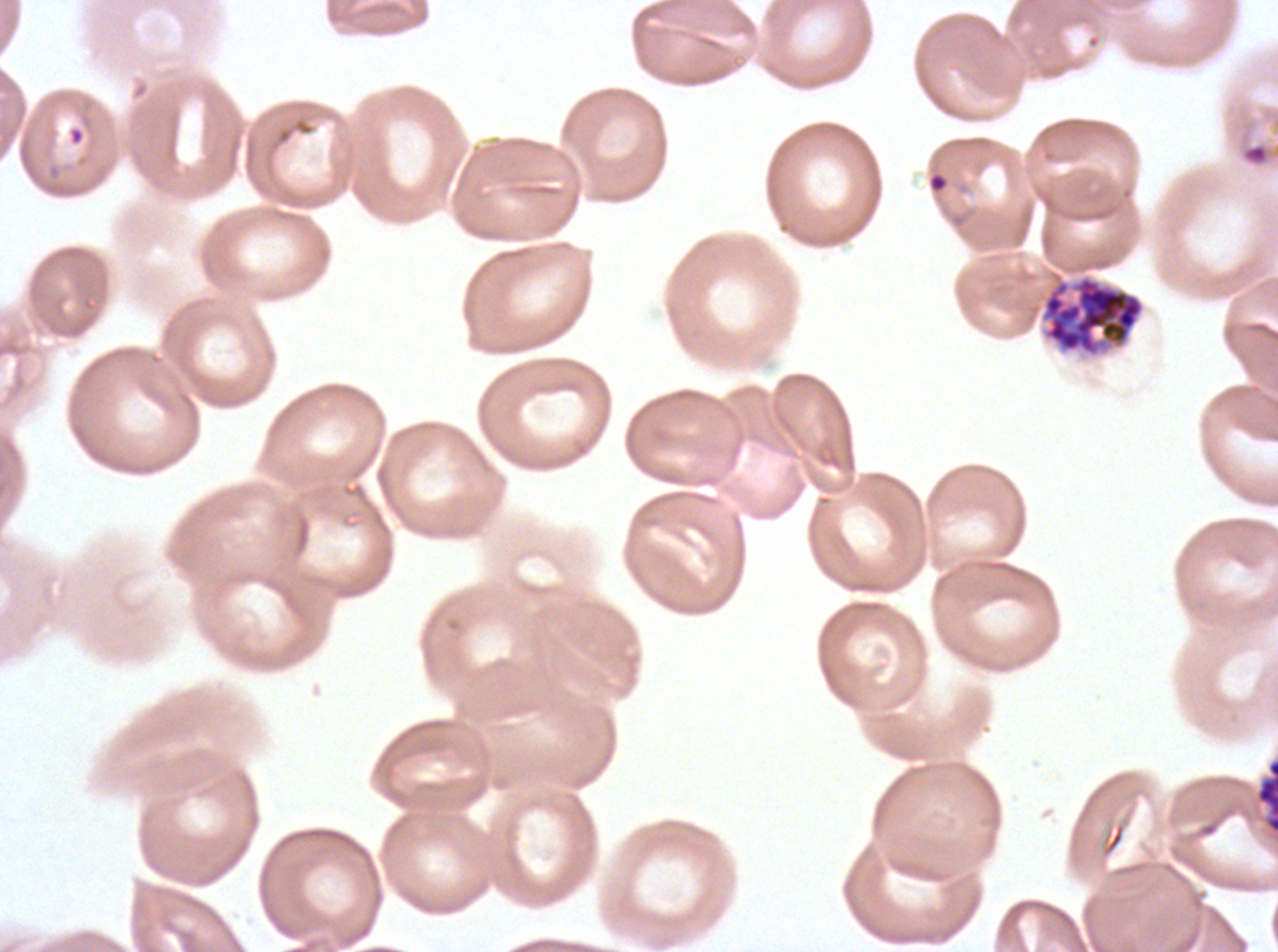

Approximate bounding boxes as {x1, y1, x2, y2} in pixels. Late schizont locations: {1255, 758, 1277, 835}. Ring locations: {927, 171, 949, 194}. Debris locations: {1238, 140, 1277, 169}. Segmenter locations: {1039, 271, 1146, 359}. Thin blood smear. Life-cycle stages observed: ring, late schizont, segmenter. Giemsa stain. Ex-vivo Plasmodium falciparum culture from a patient in The Gambia, grown for 24 to 48 hours. Image is 1278×952 pixels. One sub-image of a larger composite.